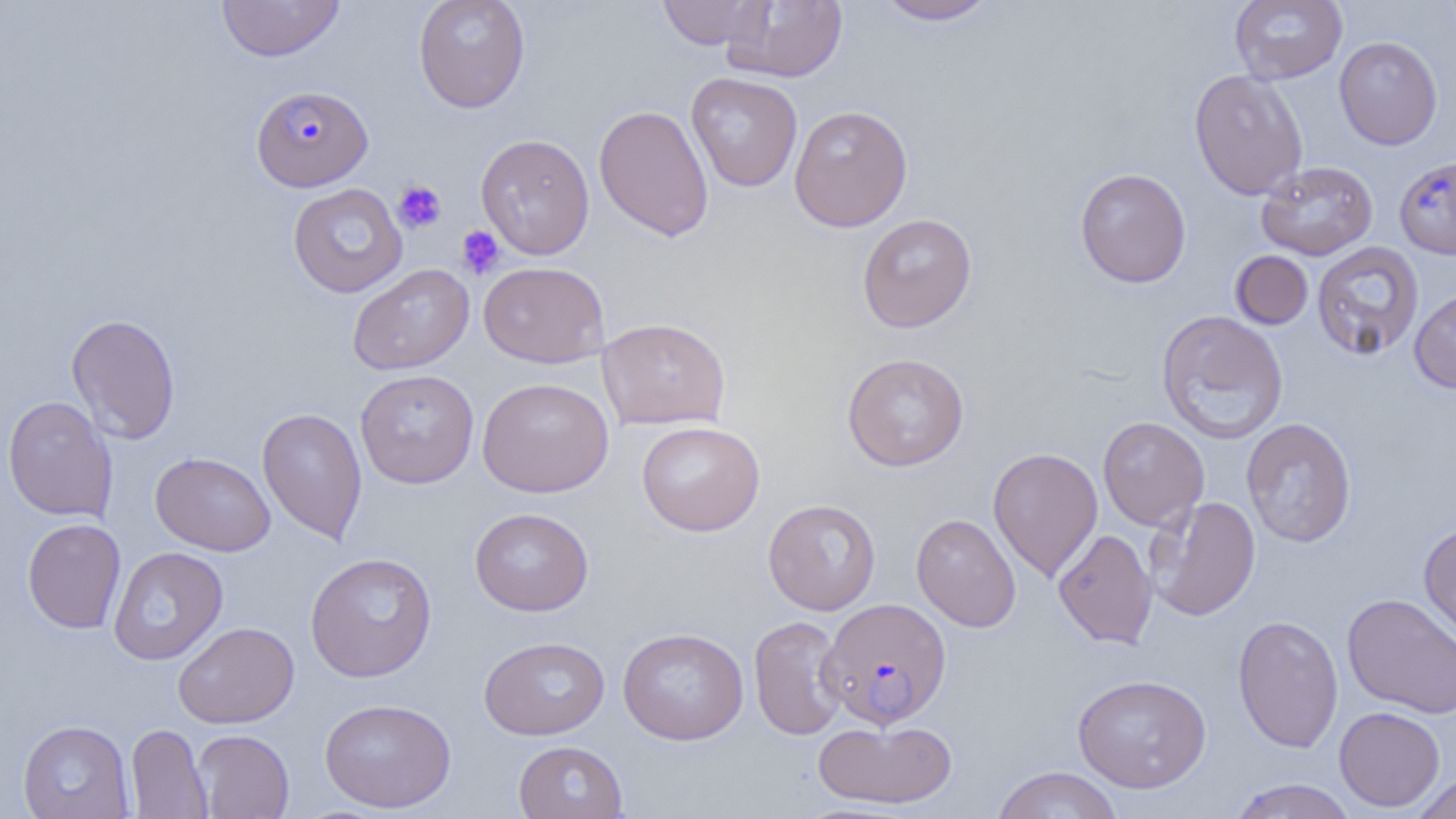

Approximate bounding boxes as named x1/y1/x2/y2 corners in pixels. Platelet locations: (x1=393, y1=181, x2=447, y2=233), (x1=456, y1=226, x2=505, y2=279). Uninfected red blood cell locations: (x1=216, y1=0, x2=346, y2=62), (x1=412, y1=0, x2=531, y2=113), (x1=657, y1=0, x2=771, y2=50), (x1=723, y1=0, x2=848, y2=83), (x1=873, y1=0, x2=999, y2=25), (x1=1229, y1=0, x2=1347, y2=84), (x1=1333, y1=36, x2=1443, y2=150), (x1=1189, y1=68, x2=1308, y2=200), (x1=686, y1=72, x2=803, y2=192), (x1=594, y1=104, x2=714, y2=242), (x1=788, y1=104, x2=913, y2=232), (x1=476, y1=133, x2=595, y2=259), (x1=1256, y1=161, x2=1378, y2=261), (x1=1074, y1=168, x2=1192, y2=288), (x1=287, y1=183, x2=408, y2=298), (x1=857, y1=213, x2=978, y2=333), (x1=1311, y1=242, x2=1424, y2=361), (x1=1230, y1=250, x2=1313, y2=330), (x1=479, y1=261, x2=610, y2=367), (x1=348, y1=263, x2=474, y2=375), (x1=1409, y1=287, x2=1456, y2=394), (x1=1156, y1=309, x2=1288, y2=445), (x1=65, y1=313, x2=181, y2=444), (x1=597, y1=317, x2=731, y2=430), (x1=842, y1=352, x2=970, y2=471), (x1=355, y1=369, x2=479, y2=489), (x1=476, y1=377, x2=614, y2=498), (x1=3, y1=395, x2=118, y2=522), (x1=257, y1=407, x2=368, y2=545), (x1=1097, y1=416, x2=1209, y2=530), (x1=1241, y1=417, x2=1357, y2=548), (x1=636, y1=421, x2=765, y2=536), (x1=988, y1=447, x2=1103, y2=582), (x1=150, y1=451, x2=276, y2=556), (x1=1145, y1=496, x2=1262, y2=621), (x1=763, y1=498, x2=882, y2=615), (x1=469, y1=507, x2=594, y2=616), (x1=911, y1=513, x2=1021, y2=632), (x1=22, y1=518, x2=126, y2=634), (x1=1418, y1=521, x2=1456, y2=647), (x1=1053, y1=528, x2=1158, y2=648), (x1=108, y1=546, x2=228, y2=665), (x1=305, y1=551, x2=437, y2=682), (x1=1341, y1=592, x2=1456, y2=719), (x1=1232, y1=614, x2=1344, y2=753), (x1=749, y1=615, x2=849, y2=740), (x1=173, y1=621, x2=299, y2=728), (x1=618, y1=627, x2=749, y2=745), (x1=479, y1=636, x2=610, y2=740), (x1=1072, y1=673, x2=1212, y2=793), (x1=319, y1=697, x2=456, y2=813), (x1=1334, y1=707, x2=1445, y2=812), (x1=813, y1=718, x2=959, y2=809), (x1=17, y1=720, x2=134, y2=819), (x1=126, y1=723, x2=212, y2=818), (x1=192, y1=729, x2=294, y2=818), (x1=513, y1=740, x2=628, y2=819), (x1=990, y1=765, x2=1122, y2=818), (x1=1411, y1=772, x2=1456, y2=819), (x1=1228, y1=778, x2=1358, y2=819). Plasmodium falciparum-infected red blood cell locations: (x1=251, y1=84, x2=373, y2=190), (x1=1394, y1=156, x2=1456, y2=261), (x1=819, y1=598, x2=951, y2=728). Slide-level diagnosis: Plasmodium falciparum. One field of a larger specimen. Thin blood film. Light microscopy. Image is 1456×819 pixels. Captured at 1000x magnification.